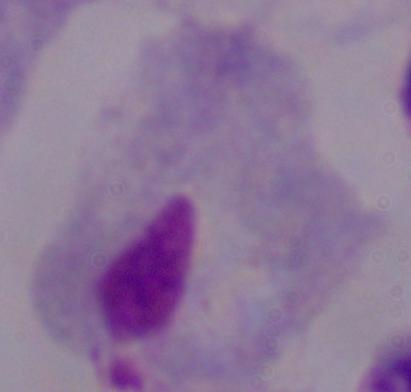
A trichomonad is seen. Captured at 1000x magnification. Micrograph.